Report the malaria status of this cell.
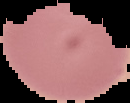

Uninfected.

Cell region segmented out of the field of view; the surrounding area is masked to black. From a thin blood smear. Image is 130×103 pixels.